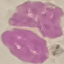

{
  "malaria_status": "uninfected",
  "image_type": "cell patch, automatically extracted from a larger field of view and resized to 64 × 64 pixels",
  "capture": "smartphone through the microscope eyepiece",
  "stain": "Giemsa",
  "preparation": "thin blood smear"
}